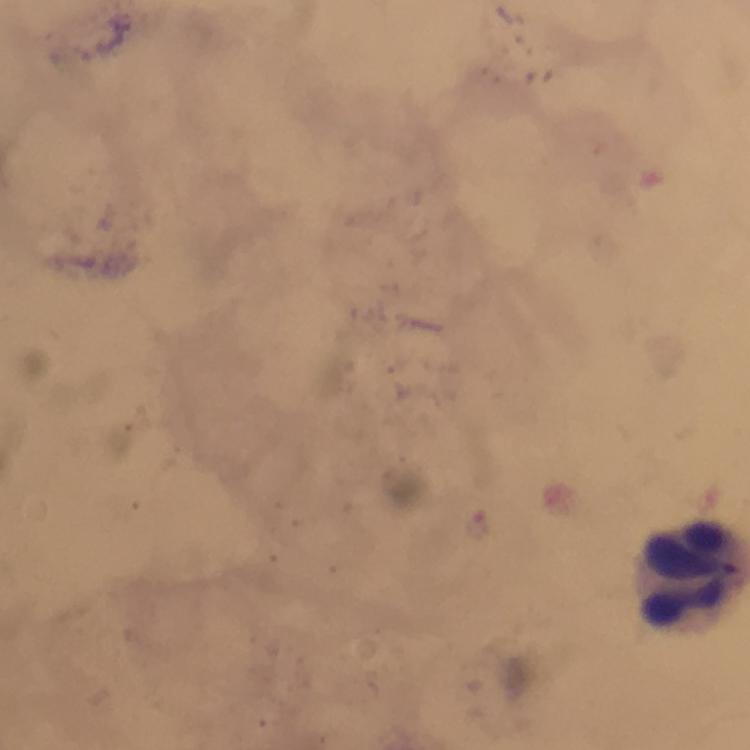
capture = smartphone mounted on the microscope
image size = 750×750 pixels
magnification = 100x
leukocyte locations = approximate centers as {x, y} in pixels: {689, 573}
Plasmodium parasites = none detected
preparation = thick blood smear
stain = Giemsa
immersion oil = used
context = from a diagnostic examination for malaria
cropped from = one field of view